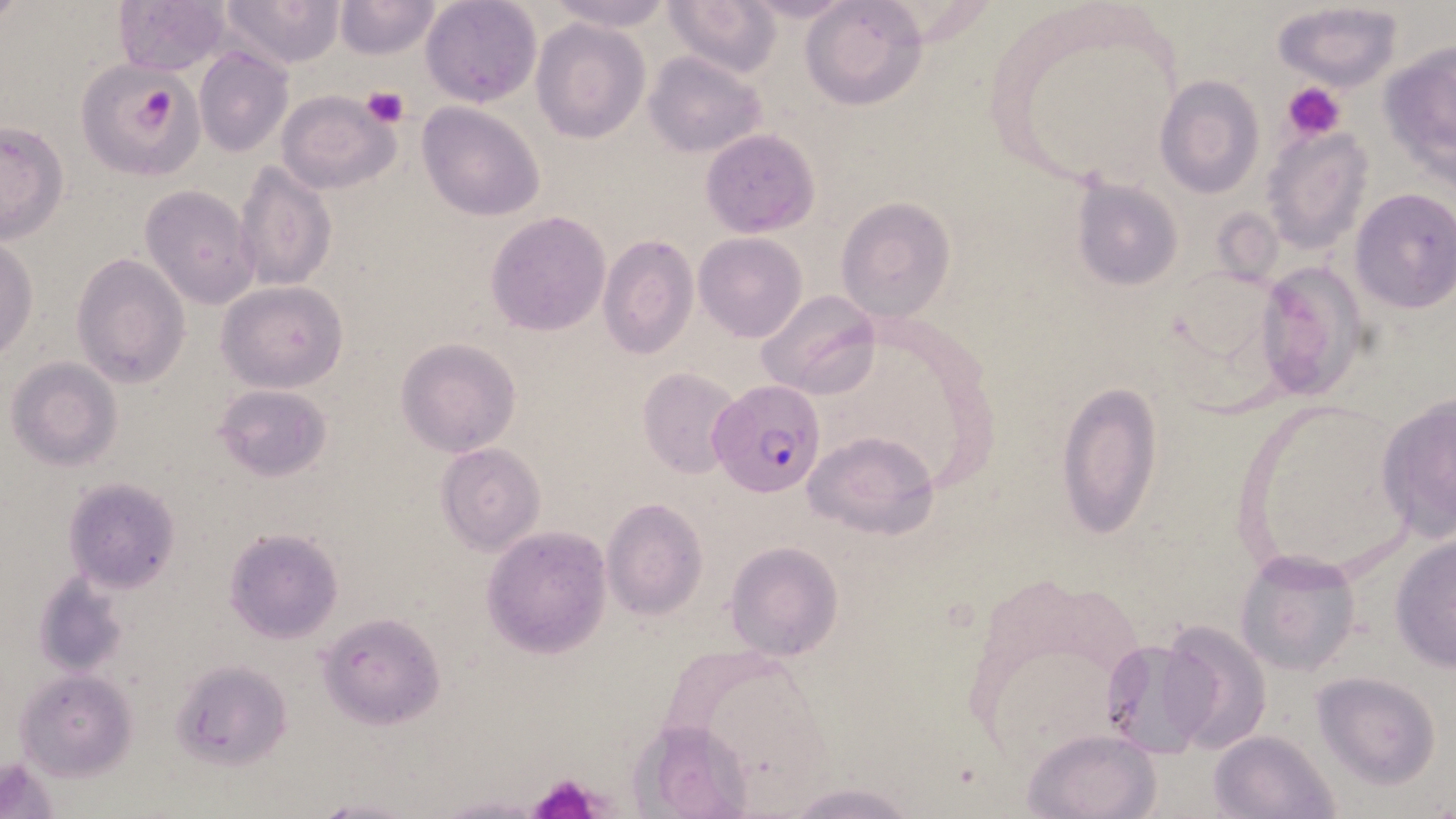
Summary:
  - Coordinate format: approximate bounding boxes as named x1/y1/x2/y2 corners in pixels
  - Plasmodium falciparum-infected red blood cell locations: (x1=708, y1=378, x2=827, y2=499)
  - Platelet locations: (x1=128, y1=81, x2=184, y2=147), (x1=1286, y1=82, x2=1345, y2=142), (x1=361, y1=87, x2=408, y2=128), (x1=531, y1=772, x2=603, y2=819)
  - Uninfected red blood cell locations: (x1=113, y1=0, x2=233, y2=77), (x1=220, y1=0, x2=344, y2=71), (x1=420, y1=0, x2=541, y2=108), (x1=664, y1=0, x2=781, y2=76), (x1=738, y1=0, x2=859, y2=25), (x1=799, y1=0, x2=927, y2=112), (x1=333, y1=1, x2=443, y2=60), (x1=545, y1=1, x2=675, y2=32), (x1=1272, y1=4, x2=1403, y2=93), (x1=532, y1=18, x2=650, y2=143), (x1=1378, y1=36, x2=1453, y2=178), (x1=194, y1=48, x2=292, y2=158), (x1=644, y1=51, x2=766, y2=157), (x1=88, y1=70, x2=205, y2=176), (x1=1155, y1=76, x2=1264, y2=199), (x1=277, y1=89, x2=399, y2=193), (x1=417, y1=103, x2=545, y2=221), (x1=205, y1=117, x2=313, y2=264), (x1=0, y1=121, x2=69, y2=242), (x1=1262, y1=128, x2=1372, y2=254), (x1=700, y1=130, x2=818, y2=239), (x1=233, y1=157, x2=336, y2=293), (x1=1071, y1=179, x2=1183, y2=290), (x1=140, y1=184, x2=259, y2=309), (x1=1349, y1=188, x2=1456, y2=315), (x1=835, y1=198, x2=957, y2=323), (x1=485, y1=212, x2=611, y2=337), (x1=694, y1=232, x2=808, y2=343), (x1=597, y1=235, x2=698, y2=360), (x1=0, y1=238, x2=38, y2=362), (x1=72, y1=254, x2=191, y2=390), (x1=1255, y1=259, x2=1371, y2=403), (x1=217, y1=280, x2=348, y2=391), (x1=755, y1=290, x2=879, y2=402), (x1=396, y1=338, x2=521, y2=457), (x1=5, y1=357, x2=123, y2=471), (x1=638, y1=366, x2=745, y2=479), (x1=1057, y1=382, x2=1165, y2=542), (x1=213, y1=384, x2=333, y2=482), (x1=1377, y1=391, x2=1456, y2=543), (x1=802, y1=429, x2=939, y2=538), (x1=436, y1=442, x2=545, y2=553), (x1=61, y1=476, x2=180, y2=593), (x1=601, y1=498, x2=708, y2=620), (x1=482, y1=527, x2=611, y2=659), (x1=225, y1=528, x2=342, y2=642), (x1=1390, y1=530, x2=1456, y2=672), (x1=724, y1=540, x2=844, y2=661), (x1=1233, y1=549, x2=1362, y2=677), (x1=33, y1=573, x2=133, y2=679), (x1=317, y1=611, x2=446, y2=728), (x1=1155, y1=618, x2=1273, y2=755), (x1=1098, y1=636, x2=1219, y2=757), (x1=170, y1=659, x2=293, y2=771), (x1=15, y1=670, x2=137, y2=779), (x1=1311, y1=672, x2=1441, y2=789), (x1=1022, y1=727, x2=1160, y2=819), (x1=1209, y1=730, x2=1340, y2=818), (x1=0, y1=755, x2=63, y2=819), (x1=785, y1=782, x2=921, y2=819), (x1=306, y1=792, x2=429, y2=819), (x1=432, y1=794, x2=548, y2=818)
  - Slide-level diagnosis: Plasmodium falciparum
  - Field of view: one of a larger specimen
  - Preparation: thin blood film
  - Image size: 1456×819 pixels
  - Magnification: 1000x
  - Modality: optical microscopy
  - Stain: May-Grünwald-Giemsa